Comment on the morphology of the erythrocytes.
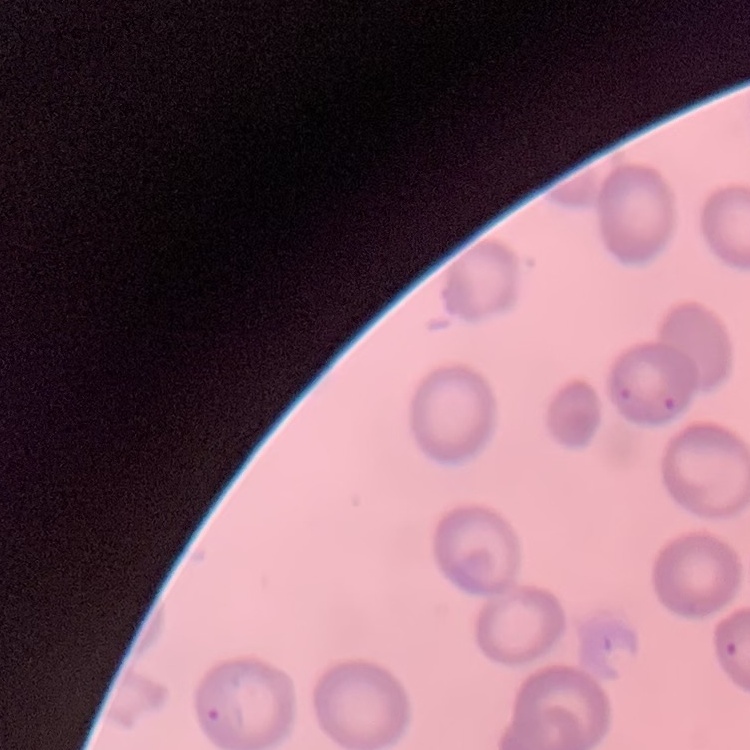

They show no rouleaux formation.

{
  "preparation": "thin blood film",
  "stain": "Field's or Giemsa",
  "image_type": "square crop of a larger photomicrograph"
}